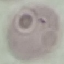
result = no malaria parasites detected
capture = smartphone camera at the microscope eyepiece
preparation = thin smear
image type = cell patch, automatically extracted from a larger field of view and resized to 64 × 64 pixels
stain = Giemsa